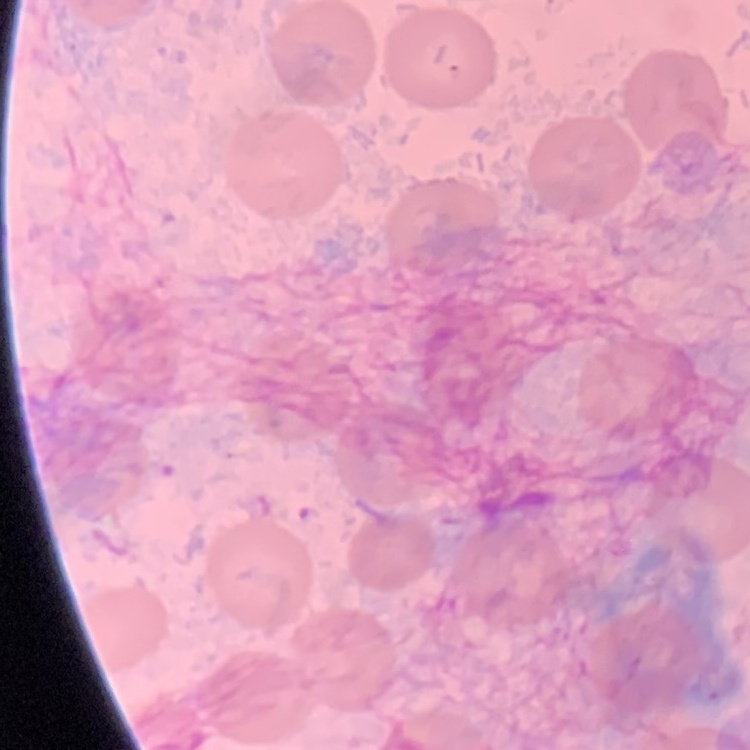
erythrocyte morphology = no rouleaux formation
preparation = thin peripheral smear
stain = Field's or Giemsa
image type = square crop of a larger photomicrograph